Name the parasite shown.
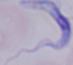

A trypanosome.

Summary:
  - Modality: micrograph
  - Magnification: 1000x